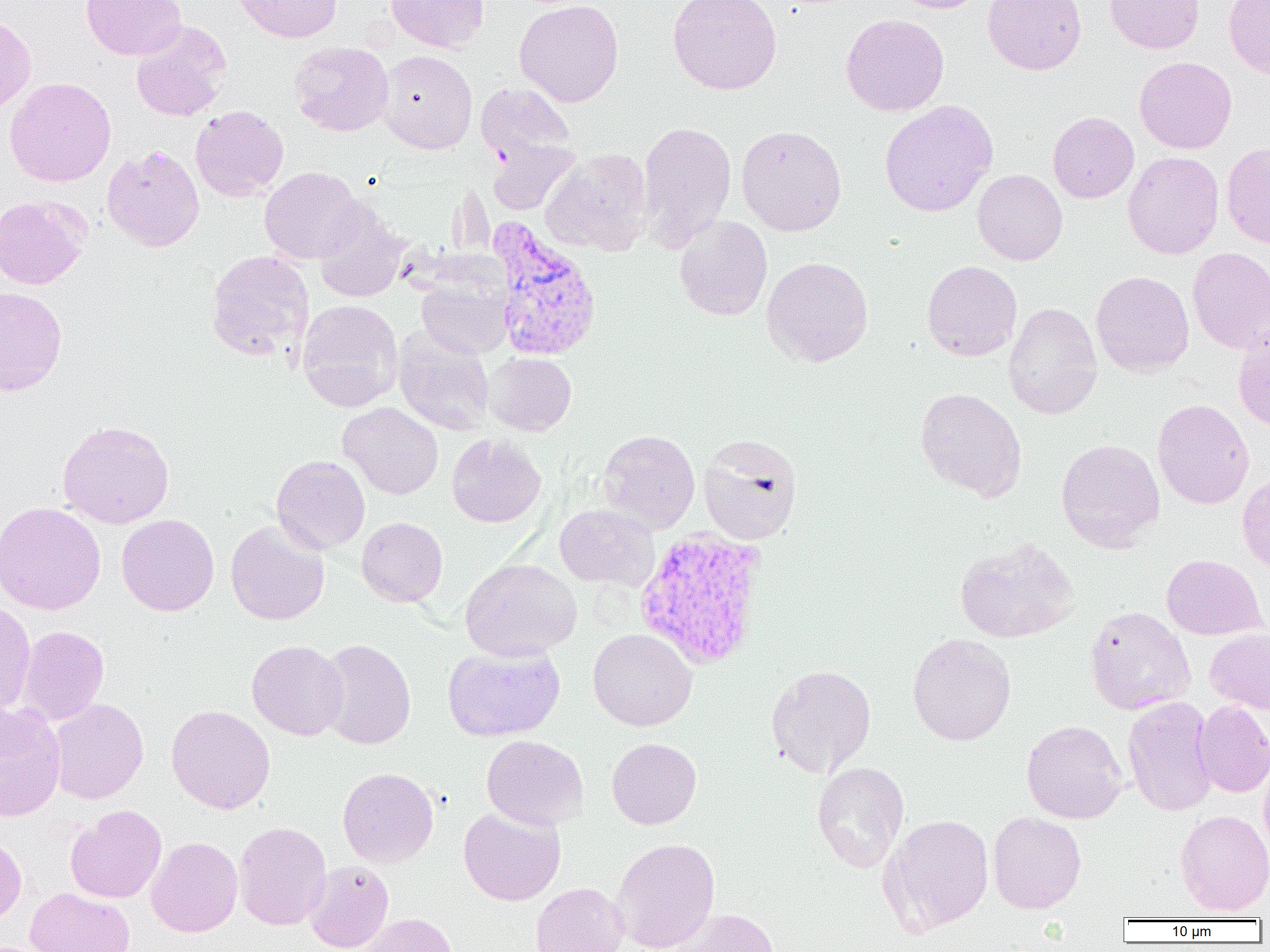
Approximate bounding boxes as [x1, y1, x2, y2] in pixels. Uninfected red blood cell locations: [81, 0, 186, 61], [234, 0, 342, 43], [386, 0, 489, 53], [514, 0, 624, 107], [668, 0, 782, 95], [890, 0, 992, 13], [982, 0, 1087, 75], [1105, 0, 1205, 54], [1223, 0, 1270, 79], [840, 14, 949, 116], [0, 15, 36, 117], [131, 22, 232, 121], [288, 41, 394, 137], [376, 50, 477, 153], [1134, 56, 1237, 154], [4, 77, 116, 187], [475, 83, 575, 165], [879, 100, 998, 217], [190, 105, 288, 201], [1048, 112, 1139, 203], [637, 120, 736, 249], [736, 124, 847, 236], [487, 138, 581, 215], [1221, 142, 1270, 249], [102, 145, 204, 251], [541, 149, 654, 256], [1123, 151, 1224, 259], [259, 167, 363, 264], [972, 169, 1067, 265], [0, 194, 91, 289], [313, 200, 409, 302], [673, 216, 772, 321], [1187, 247, 1270, 354], [205, 249, 314, 361], [762, 256, 873, 367], [922, 260, 1022, 361], [1091, 271, 1194, 377], [416, 277, 512, 359], [0, 287, 67, 397], [296, 299, 403, 411], [1003, 302, 1102, 419], [1233, 327, 1270, 431], [393, 328, 495, 436], [483, 352, 576, 436], [915, 387, 1027, 502], [1152, 399, 1254, 509], [338, 402, 444, 499], [58, 420, 174, 529], [598, 429, 700, 533], [446, 433, 546, 527], [698, 433, 803, 545], [1056, 438, 1165, 552], [272, 454, 370, 554], [1236, 471, 1270, 573], [0, 502, 106, 615], [554, 504, 660, 591], [116, 514, 219, 616], [356, 517, 448, 607], [225, 520, 329, 625], [954, 537, 1080, 643], [1161, 554, 1267, 640], [460, 558, 582, 661], [0, 600, 36, 716], [1084, 606, 1196, 716], [18, 626, 109, 725], [588, 628, 697, 731], [1204, 628, 1270, 714], [907, 633, 1016, 746], [317, 639, 416, 750], [247, 640, 348, 741], [442, 643, 565, 741], [765, 664, 877, 778], [1122, 695, 1218, 817], [49, 698, 148, 804], [1193, 700, 1270, 797], [0, 702, 66, 821], [166, 705, 275, 814], [1021, 720, 1127, 823], [481, 735, 588, 829], [606, 737, 702, 829], [1259, 755, 1270, 860], [812, 761, 910, 872], [338, 767, 438, 867], [66, 804, 167, 903], [458, 806, 566, 905], [1175, 809, 1270, 916], [987, 811, 1086, 913], [880, 814, 994, 934], [233, 821, 332, 930], [0, 836, 27, 925], [146, 836, 243, 937], [610, 837, 720, 952], [304, 860, 394, 952], [530, 882, 628, 952], [26, 887, 135, 952], [671, 908, 780, 952], [361, 913, 457, 952]. Plasmodium vivax-infected red blood cell locations: [488, 218, 603, 363], [633, 528, 769, 671]. Slide-level diagnosis: Plasmodium vivax. Thin blood film. Captured at 1000x magnification. Optical microscopy. One field of a larger specimen. Image is 1270×952 pixels.